Comment on the morphology of the red blood cells.
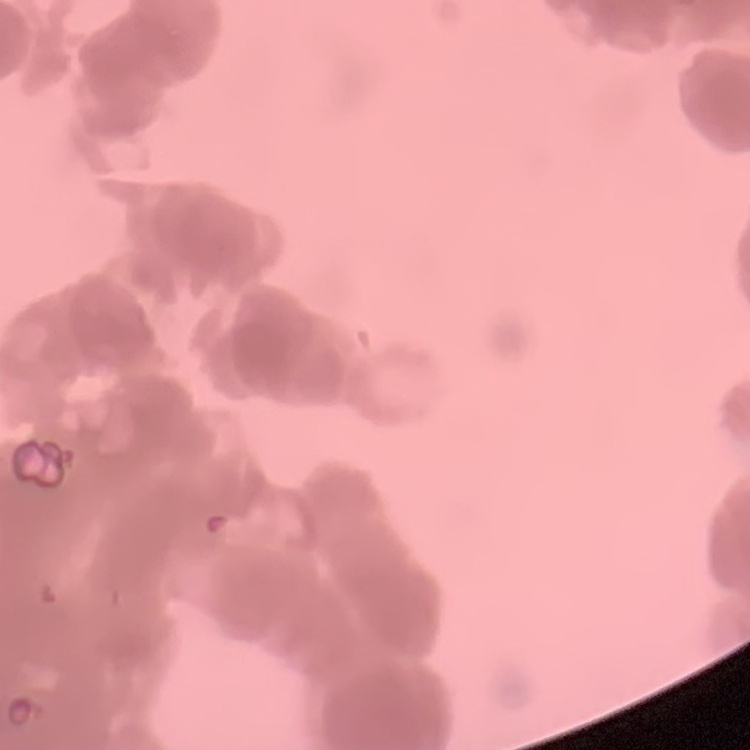
They show rouleaux formation.

{
  "preparation": "thin peripheral smear",
  "image_type": "square crop of a larger photomicrograph",
  "stain": "Field's or Giemsa"
}